Name the cell type shown.
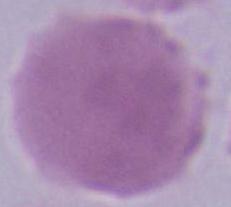

This is an erythrocyte.

Summary:
  - Magnification: 1000x
  - Modality: photomicrograph